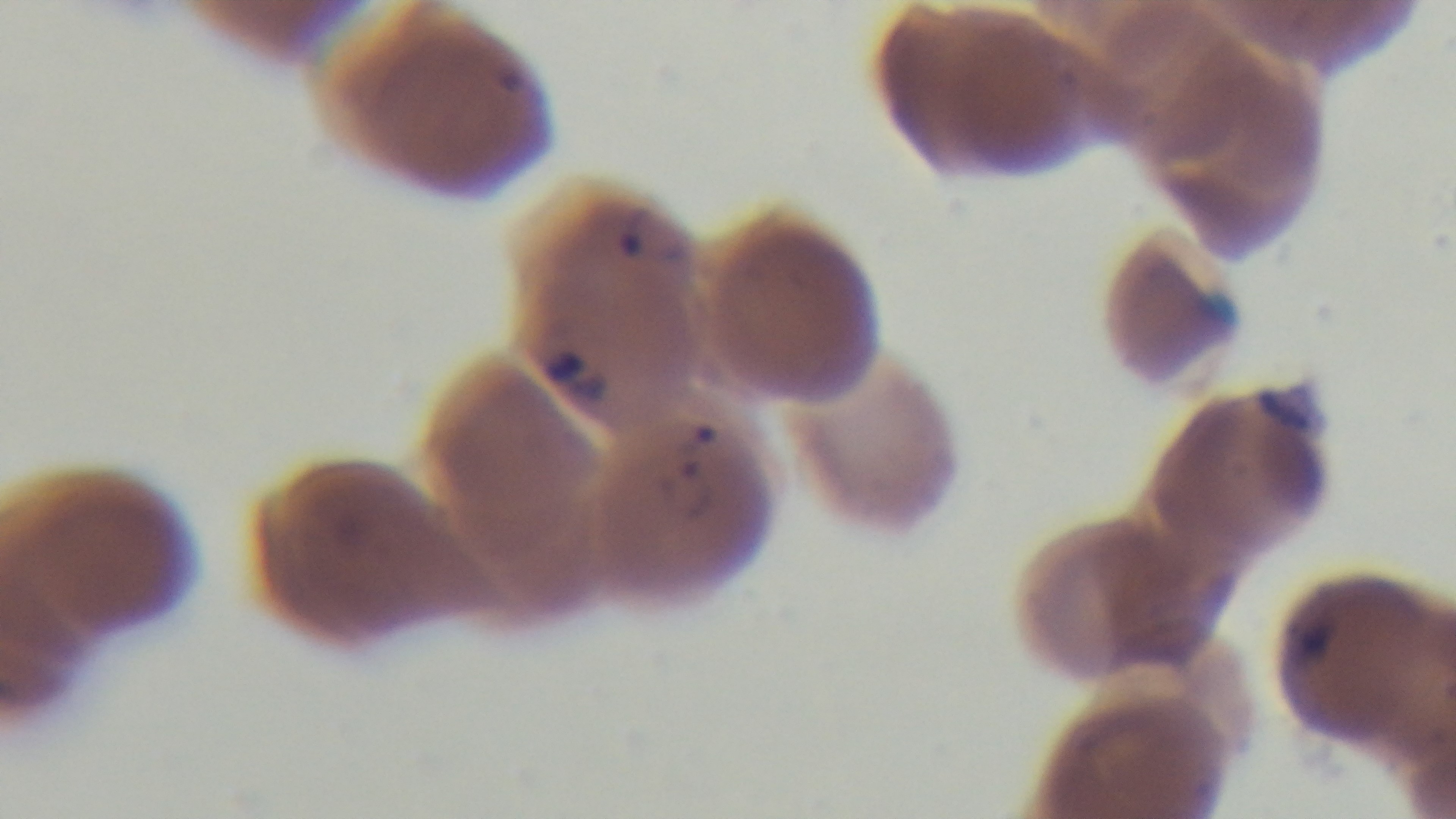

Summary:
  - Objective: 100x oil immersion
  - Modality: light microscopy
  - Stain: Giemsa
  - Capture: mounted 4K digital camera
  - Malaria status: infected
  - Preparation: thin
  - Field of view: one from the slide